Report the malaria status of this cell.
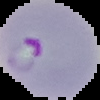
Parasitized.

Summary:
  - Image size: 100×100 pixels
  - Preparation: thin blood smear
  - Image type: segmented cell region with the area outside set to black